Comment on the morphology of the red blood cells.
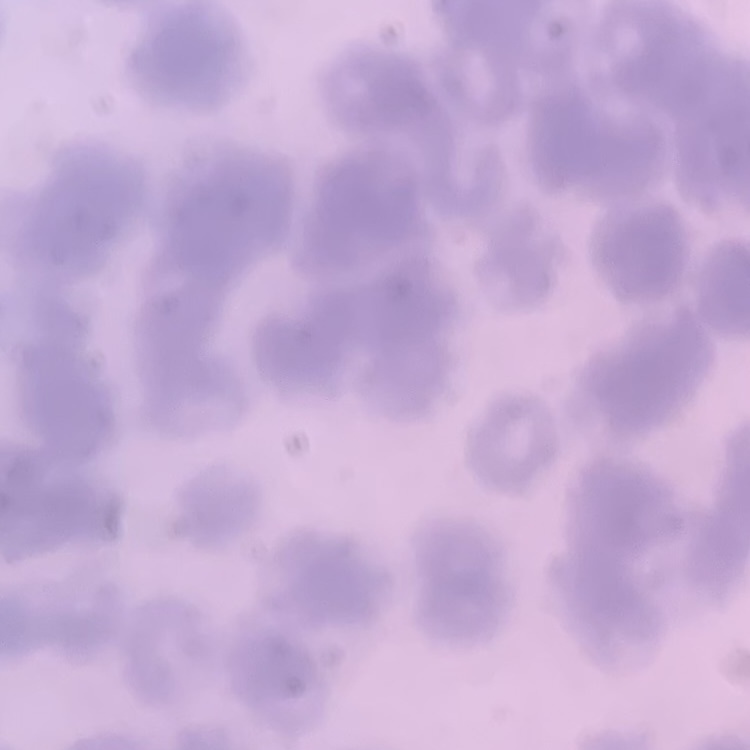
They show rouleaux formation.

One tile cut from a larger photomicrograph. Stained with either Field's or Giemsa. Thin blood film.